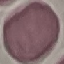
Summary:
  - Result: no malaria parasites detected
  - Image type: cell patch, automatically extracted from a larger field of view and resized to 64 × 64 pixels
  - Preparation: thin smear
  - Stain: Giemsa
  - Capture: smartphone through the microscope eyepiece